Locate every blood parasite and identify its species.
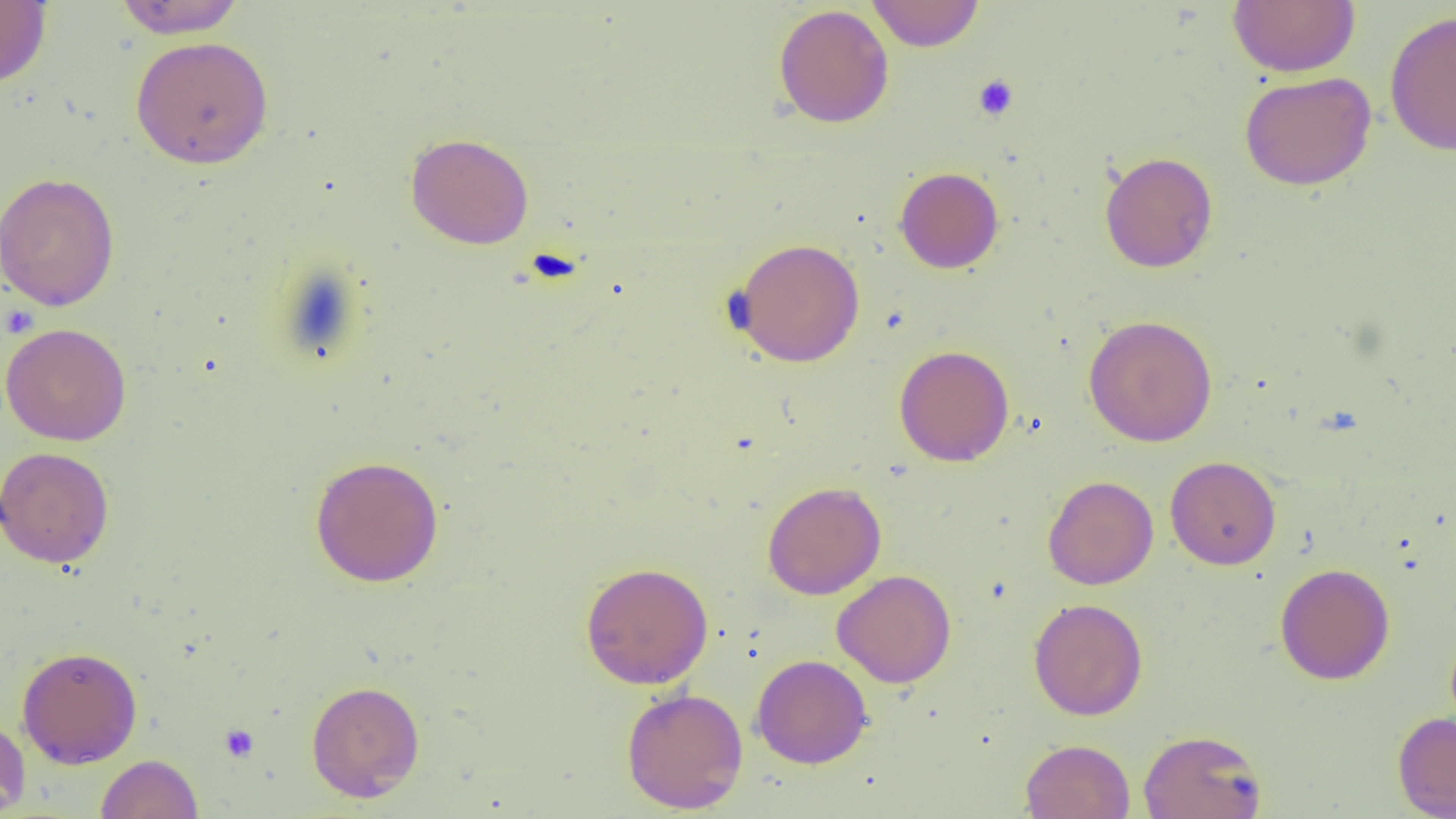

No blood parasites observed.

Summary:
  - Coordinate format: approximate bounding boxes as (x1, y1, x2, y2) in pixels
  - Uninfected red blood cell locations: (112, 0, 248, 38), (867, 0, 984, 51), (1227, 0, 1360, 77), (0, 2, 52, 88), (773, 4, 894, 129), (1385, 10, 1456, 157), (130, 36, 274, 169), (1239, 71, 1377, 190), (405, 133, 534, 249), (1099, 151, 1218, 273), (895, 167, 1004, 273), (0, 172, 120, 311), (732, 238, 866, 367), (1083, 314, 1218, 447), (1, 322, 131, 446), (894, 344, 1014, 467), (0, 446, 115, 568), (309, 455, 444, 587), (1165, 455, 1281, 570), (1042, 475, 1159, 590), (761, 481, 886, 599), (580, 561, 714, 689), (1275, 563, 1395, 685), (832, 569, 956, 688), (1028, 598, 1148, 720), (17, 646, 143, 769), (751, 654, 873, 769), (306, 680, 425, 802), (621, 686, 749, 814), (1392, 711, 1456, 818), (0, 713, 31, 817), (1138, 728, 1268, 819), (1020, 738, 1136, 819), (95, 754, 203, 819)
  - Platelet locations: (973, 74, 1019, 121), (219, 723, 259, 762)
  - Slide-level diagnosis: negative for blood parasites
  - Magnification: 1000x
  - Field of view: one of a larger specimen
  - Modality: optical microscopy
  - Preparation: thin blood film
  - Image size: 1456×819 pixels